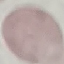

Summary:
  - Malaria status: uninfected
  - Stain: Giemsa
  - Preparation: thin blood film
  - Image type: cell patch, automatically extracted from a larger field of view and resized to 64 × 64 pixels
  - Capture: smartphone camera at the microscope eyepiece